Outline each blood parasite and name the species.
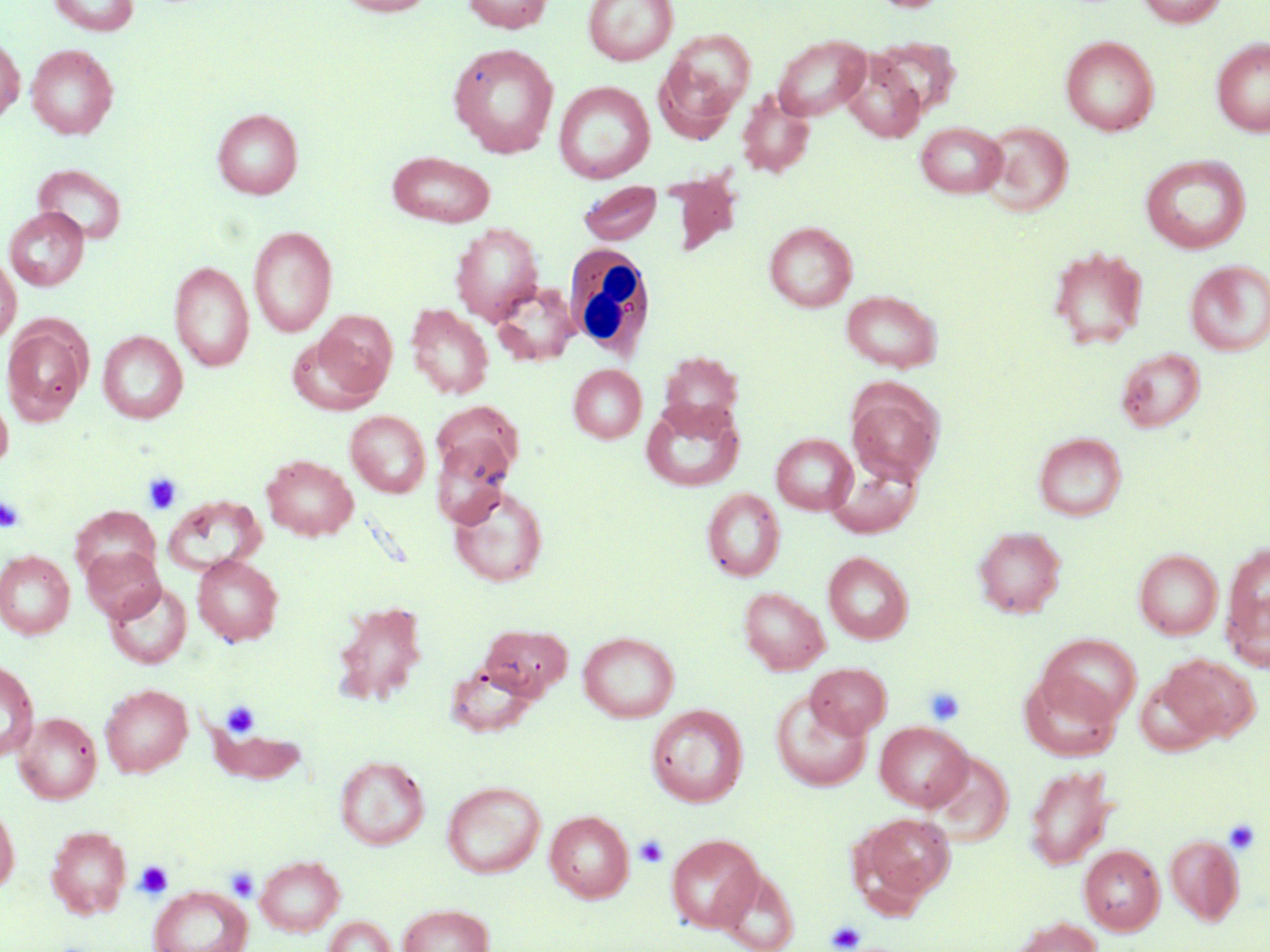
No blood parasites observed.

slide-level diagnosis = negative for blood parasites
magnification = 1000x
stain = May-Grünwald-Giemsa
platelet locations = approximate bounding boxes as [x1, y1, x2, y2] in pixels: [142, 472, 183, 515], [0, 495, 25, 533], [923, 686, 966, 726], [221, 700, 260, 738], [1223, 818, 1260, 854], [634, 835, 669, 867], [134, 860, 174, 899], [226, 867, 259, 901], [826, 920, 866, 951]
preparation = thin blood film
modality = optical microscopy
field of view = single
uninfected red blood cell locations = approximate bounding boxes as [x1, y1, x2, y2] in pixels: [48, 0, 141, 36], [335, 0, 435, 16], [462, 0, 553, 34], [583, 0, 678, 65], [1136, 0, 1227, 27], [658, 29, 755, 130], [0, 34, 24, 124], [772, 35, 871, 120], [1060, 35, 1159, 136], [872, 37, 959, 118], [1212, 37, 1270, 137], [448, 43, 559, 157], [26, 44, 118, 139], [840, 53, 926, 143], [554, 81, 655, 183], [736, 90, 815, 179], [212, 108, 303, 199], [915, 121, 1008, 197], [980, 121, 1073, 216], [388, 151, 496, 227], [1140, 154, 1251, 254], [32, 164, 127, 245], [663, 172, 742, 256], [578, 181, 663, 245], [4, 206, 89, 291], [764, 221, 857, 312], [450, 222, 544, 324], [248, 226, 337, 337], [1047, 245, 1150, 349], [0, 253, 20, 345], [169, 260, 254, 372], [1185, 260, 1270, 356], [490, 282, 578, 367], [842, 290, 942, 372], [406, 304, 494, 400], [315, 311, 397, 396], [2, 317, 93, 425], [98, 331, 188, 423], [287, 333, 383, 416], [1115, 347, 1205, 432], [658, 351, 745, 433], [568, 364, 646, 443], [845, 380, 944, 484], [0, 389, 13, 475], [641, 399, 743, 492], [432, 400, 524, 485], [345, 410, 431, 498], [1033, 431, 1127, 521], [771, 433, 857, 514], [431, 438, 514, 528], [262, 454, 358, 541], [826, 458, 922, 538], [449, 484, 549, 587], [702, 488, 785, 581], [164, 494, 266, 577], [71, 506, 161, 586], [973, 526, 1067, 619], [1222, 543, 1270, 662], [81, 546, 165, 622], [1134, 549, 1223, 639], [0, 551, 74, 639], [823, 551, 913, 644], [193, 554, 283, 646], [104, 580, 192, 669], [738, 587, 830, 675], [333, 601, 429, 706], [479, 624, 574, 700], [579, 631, 679, 722], [1039, 633, 1142, 723], [1160, 654, 1260, 744], [0, 660, 38, 761], [446, 662, 539, 737], [806, 662, 892, 738], [1019, 671, 1122, 762], [1135, 675, 1220, 756], [100, 684, 193, 777], [770, 691, 872, 792], [646, 704, 749, 807], [196, 708, 312, 785], [12, 710, 102, 804], [875, 721, 973, 811], [927, 751, 1014, 845], [335, 755, 429, 849], [1024, 765, 1117, 870], [442, 781, 546, 878], [0, 799, 20, 895], [545, 810, 634, 902], [855, 812, 956, 906], [45, 824, 131, 919], [666, 833, 765, 933], [1165, 835, 1244, 926], [1079, 845, 1164, 935], [255, 855, 345, 936], [717, 867, 800, 952], [149, 885, 252, 952], [397, 904, 494, 952], [322, 915, 398, 952], [1011, 917, 1102, 952]
image size = 1270×952 pixels
white blood cell locations = approximate bounding boxes as [x1, y1, x2, y2] in pixels: [563, 244, 657, 360]